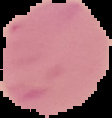
Summary:
  - Image type: cell region segmented out of the field of view; surrounding area masked to black
  - Preparation: thin blood film
  - Result: no Plasmodium parasites detected
  - Image size: 112×118 pixels